Locate every Plasmodium parasite.
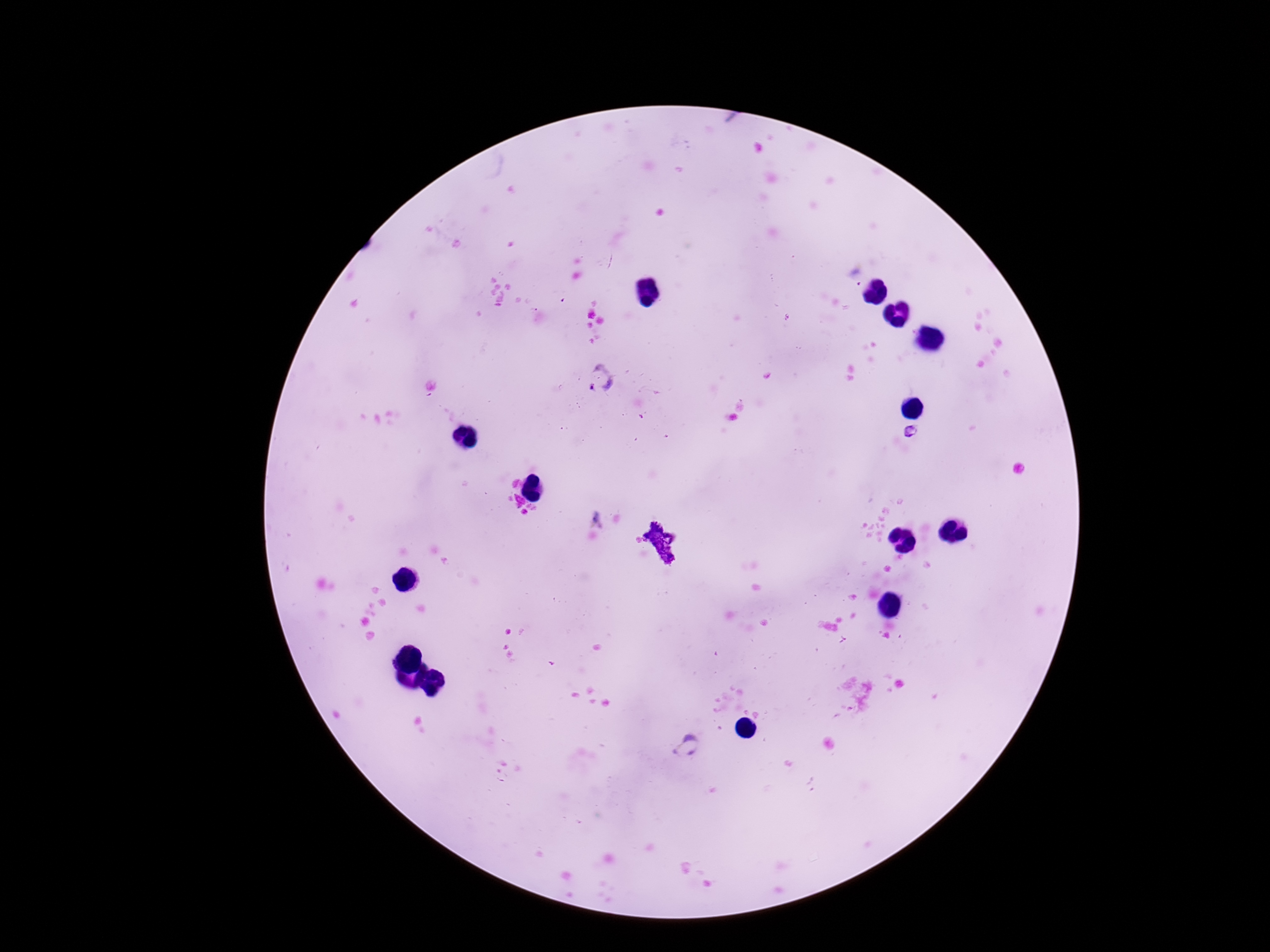

Approximate object centers, in pixels from the top-left corner.
Plasmodium parasites: (x=601, y=379), (x=686, y=748).

preparation = thick peripheral-blood smear
field of view = one from this slide
stain = Giemsa
capture = smartphone camera through the microscope eyepiece
patient malaria status = positive
magnification = 100x
image size = 1270×952 pixels